Classify this cell by malaria status.
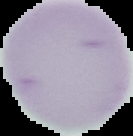

It is uninfected.

Segmented cell region on a black background. Image is 133×136 pixels. From a thin blood smear.